Identify the parasite.
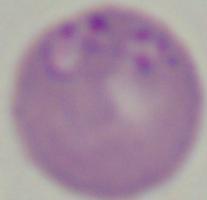

This is Babesia.

modality = photomicrograph
magnification = 1000x